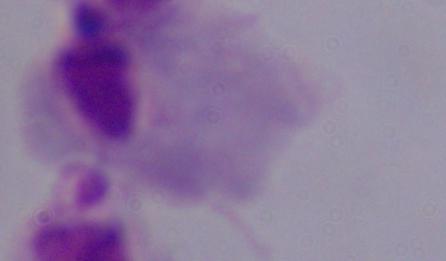 Captured at 1000x magnification. Micrograph. A trichomonad is shown.